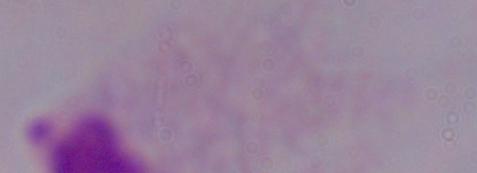
{
  "modality": "photomicrograph",
  "identification": "trichomonad",
  "magnification": "1000x"
}